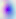
Summary:
  - Modality: micrograph
  - Magnification: 400x
  - Identification: Toxoplasma gondii